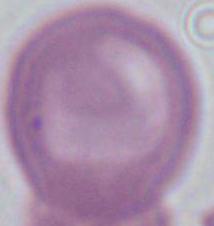

modality = micrograph
identification = erythrocyte
magnification = 1000x